Classify this cell by malaria status.
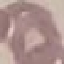
It is uninfected.

capture = smartphone camera at the microscope eyepiece
stain = Giemsa
image type = automatically extracted cell patch, resized to 64 × 64 pixels
preparation = thin blood smear